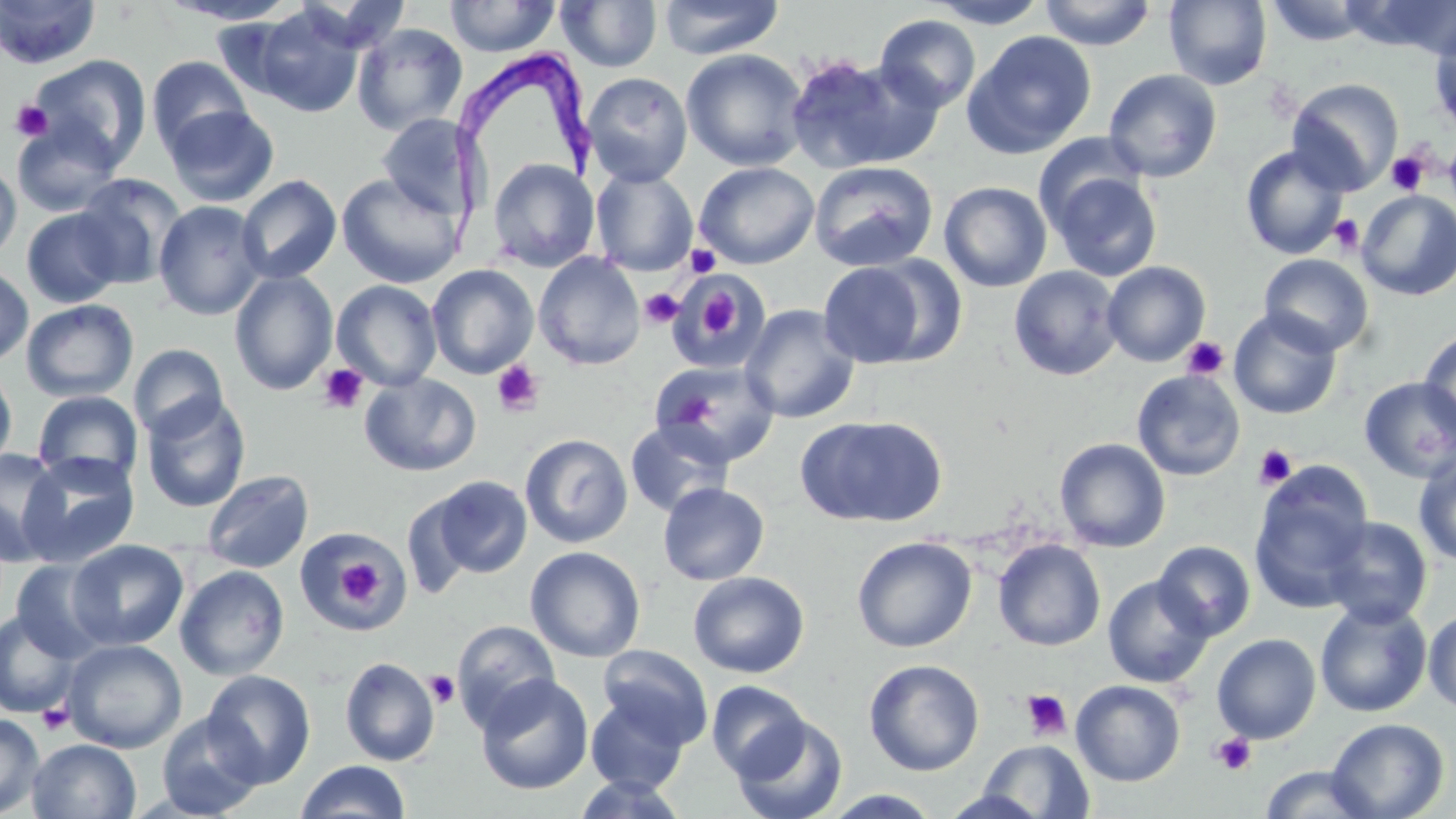
Approximate bounding boxes as (x1, y1, x2, y2) in pixels. Uninfected red blood cell locations: (1, 0, 101, 69), (157, 0, 303, 25), (444, 0, 560, 57), (924, 0, 1051, 28), (1037, 0, 1157, 50), (1165, 0, 1272, 90), (556, 1, 662, 72), (657, 1, 784, 60), (1264, 1, 1376, 46), (1350, 1, 1456, 59), (246, 4, 367, 117), (874, 14, 981, 113), (1428, 20, 1456, 134), (351, 23, 468, 136), (964, 30, 1097, 158), (681, 48, 809, 171), (28, 54, 150, 170), (784, 54, 936, 174), (146, 55, 253, 157), (1103, 69, 1222, 182), (582, 71, 693, 186), (1286, 78, 1403, 194), (165, 105, 279, 208), (377, 113, 475, 217), (11, 118, 124, 217), (1033, 132, 1146, 228), (1240, 146, 1350, 260), (487, 158, 600, 272), (0, 160, 22, 263), (810, 160, 938, 272), (694, 161, 819, 269), (591, 168, 698, 276), (337, 172, 465, 288), (1049, 172, 1163, 282), (73, 174, 188, 289), (236, 174, 342, 285), (939, 182, 1052, 292), (1356, 191, 1456, 301), (153, 200, 268, 320), (21, 208, 125, 307), (533, 252, 645, 370), (1259, 254, 1374, 357), (817, 261, 933, 368), (1102, 261, 1211, 367), (0, 264, 34, 367), (426, 264, 539, 379), (1009, 266, 1123, 381), (229, 270, 339, 395), (672, 275, 770, 370), (331, 280, 442, 391), (21, 299, 139, 402), (739, 304, 860, 424), (1229, 309, 1342, 420), (1419, 327, 1456, 440), (128, 343, 228, 441), (650, 360, 781, 468), (0, 364, 17, 473), (1132, 370, 1246, 481), (359, 372, 481, 477), (1359, 376, 1456, 483), (32, 390, 143, 486), (141, 394, 251, 512), (796, 415, 947, 528), (625, 420, 734, 518), (519, 433, 633, 548), (1054, 438, 1171, 553), (0, 448, 66, 565), (1414, 450, 1456, 567), (19, 451, 140, 567), (1250, 465, 1374, 612), (202, 469, 314, 573), (428, 475, 532, 579), (658, 482, 770, 585), (1320, 516, 1433, 628), (297, 529, 407, 633), (852, 536, 976, 653), (68, 539, 188, 651), (992, 539, 1106, 651), (1153, 541, 1255, 641), (525, 546, 646, 663), (11, 559, 113, 663), (175, 565, 290, 681), (687, 571, 810, 678), (1103, 575, 1214, 688), (1314, 599, 1432, 718), (1424, 609, 1456, 715), (0, 610, 80, 717), (452, 620, 560, 729), (1212, 634, 1321, 744), (63, 639, 187, 753), (597, 644, 713, 748), (340, 657, 440, 766), (863, 659, 985, 776), (202, 670, 315, 788), (475, 673, 593, 795), (707, 680, 811, 780), (1071, 680, 1186, 785), (585, 695, 690, 794), (156, 711, 264, 818), (0, 713, 45, 817), (732, 715, 847, 819), (1325, 717, 1449, 818), (27, 738, 142, 819), (977, 739, 1095, 818), (295, 760, 411, 818), (1259, 765, 1380, 819), (572, 773, 689, 818), (821, 789, 944, 818). Platelet locations: (10, 100, 53, 142), (1386, 151, 1430, 196), (1329, 214, 1365, 254), (686, 244, 721, 278), (639, 288, 683, 329), (699, 294, 742, 334), (1181, 336, 1229, 381), (492, 360, 545, 416), (318, 364, 369, 414), (1253, 443, 1298, 490), (337, 558, 382, 608), (425, 670, 460, 708), (1020, 688, 1072, 741), (37, 703, 74, 735), (1210, 733, 1257, 776). Trypanosoma brucei locations: (446, 41, 598, 269). Slide-level diagnosis: Trypanosoma brucei. Thin blood film. 1000x magnification. May-Grünwald-Giemsa-stained preparation. Single field of view. Image is 1456×819 pixels. Optical microscopy.